Give the extent of all uninfected red blood cells.
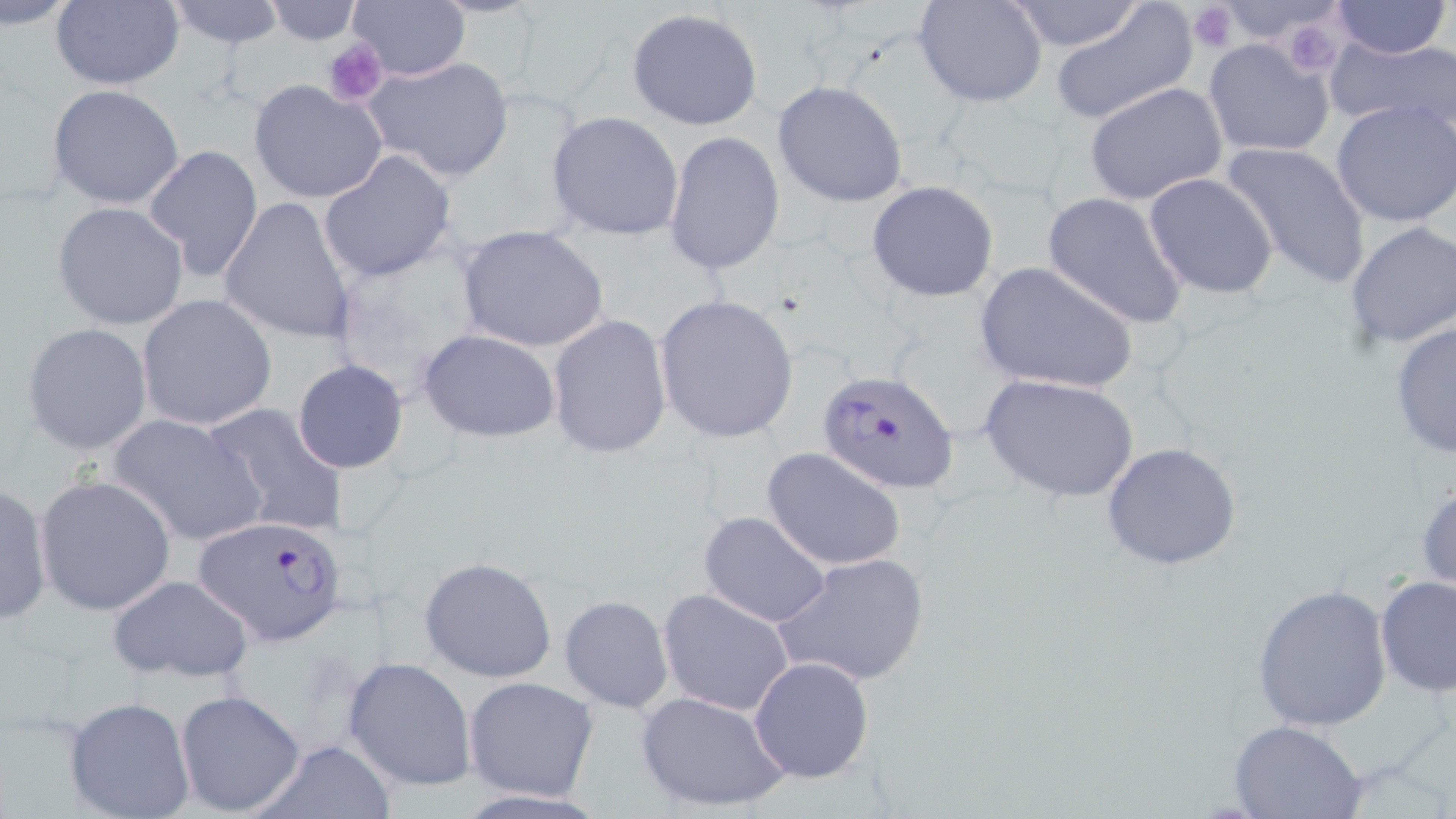
Approximate bounding boxes as [x1, y1, x2, y2] in pixels.
Uninfected red blood cells: [51, 0, 185, 90], [164, 0, 287, 51], [263, 0, 361, 45], [349, 0, 470, 82], [915, 0, 1048, 107], [1005, 0, 1147, 52], [1329, 0, 1452, 59], [6, 1, 80, 32], [1052, 2, 1197, 125], [625, 6, 764, 132], [1327, 34, 1456, 134], [1202, 37, 1335, 157], [362, 55, 513, 181], [248, 80, 388, 204], [772, 80, 909, 208], [1084, 82, 1229, 205], [47, 84, 185, 209], [1330, 99, 1456, 229], [547, 111, 684, 241], [664, 131, 785, 276], [1220, 140, 1372, 289], [143, 144, 263, 282], [317, 150, 457, 283], [1143, 172, 1280, 299], [866, 180, 1000, 303], [1043, 191, 1190, 330], [218, 197, 356, 345], [52, 201, 190, 332], [1343, 220, 1456, 351], [457, 224, 610, 354], [327, 242, 494, 397], [973, 259, 1140, 395], [135, 294, 279, 431], [656, 294, 801, 443], [546, 314, 672, 459], [1387, 317, 1455, 460], [21, 323, 153, 455], [420, 329, 562, 443], [292, 359, 408, 474], [981, 373, 1140, 503], [202, 403, 350, 538], [107, 412, 266, 547], [1100, 442, 1243, 571], [762, 446, 910, 571], [36, 474, 177, 617], [1416, 475, 1456, 597], [725, 476, 890, 613], [0, 481, 52, 627], [698, 510, 831, 628], [776, 553, 930, 687], [419, 556, 559, 684], [107, 574, 254, 685], [1374, 574, 1456, 697], [1250, 583, 1393, 732], [658, 588, 795, 717], [559, 595, 674, 713], [748, 656, 874, 783], [342, 657, 476, 792], [464, 676, 598, 800], [174, 689, 306, 817], [636, 690, 793, 815], [64, 697, 197, 818], [1228, 719, 1369, 819], [246, 738, 397, 818].

Plasmodium falciparum-infected red blood cell locations: [818, 368, 959, 493], [193, 515, 351, 647]. Platelet locations: [1185, 2, 1240, 53], [1291, 28, 1343, 75], [324, 40, 386, 106]. Slide-level diagnosis: Plasmodium falciparum. Optical microscopy. Thin blood film. One field of a larger specimen. Captured at 1000x magnification. Image is 1456×819 pixels. May-Grünwald-Giemsa-stained preparation.